Comment on the morphology of the erythrocytes.
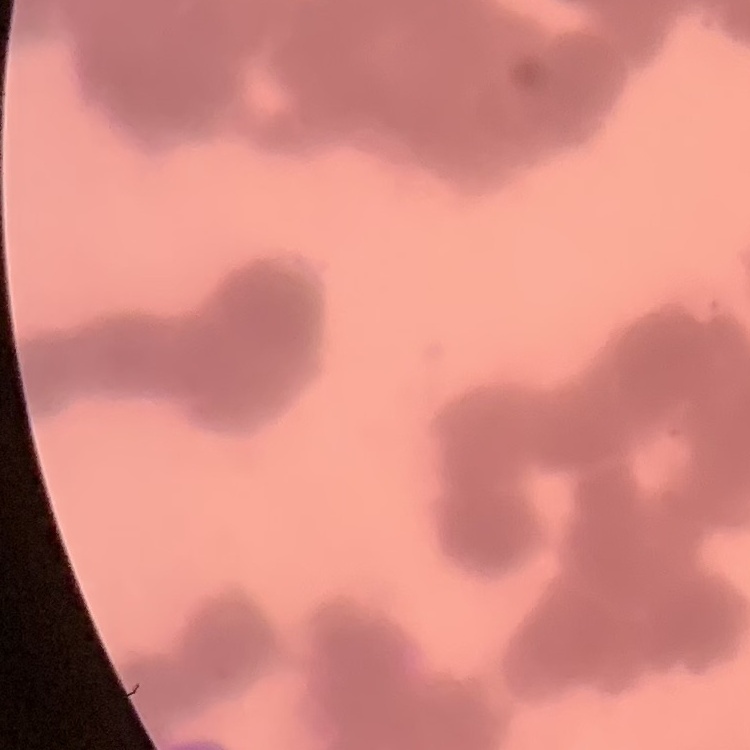
Rouleaux formation.

Thin blood film. One tile cut from a larger photomicrograph. Field's or Giemsa stain.